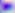
modality = photomicrograph
identification = Toxoplasma gondii
magnification = 400x